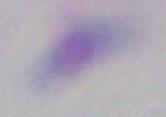
Toxoplasma gondii is shown. Captured at 1000x magnification. Photomicrograph.